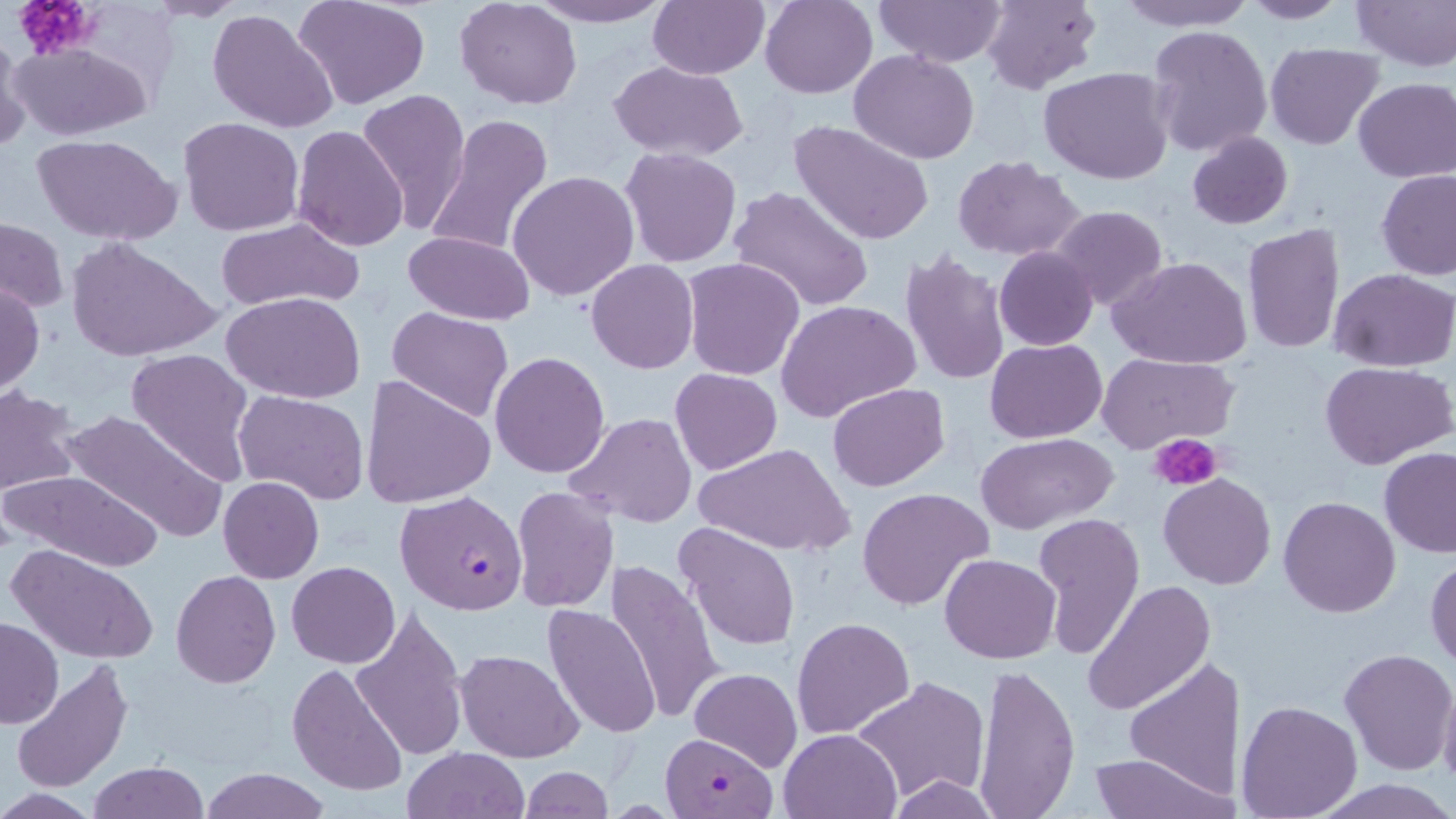 Approximate bounding boxes as (x1,y1)-(x2,y2) corner pairs in pixels. Plasmodium falciparum-infected red blood cell locations: (394,489)-(530,615), (662,732)-(775,816). Uninfected red blood cell locations: (141,0)-(247,21), (527,0)-(674,28), (648,0)-(768,79), (760,0)-(877,98), (872,0)-(1006,67), (979,0)-(1101,92), (1112,0)-(1257,30), (1351,0)-(1456,70), (293,1)-(433,111), (454,1)-(583,109), (1238,1)-(1353,23), (209,7)-(339,134), (1147,24)-(1271,157), (0,31)-(29,151), (8,41)-(154,142), (1264,42)-(1384,149), (850,50)-(980,164), (608,61)-(750,162), (1039,65)-(1173,185), (1353,78)-(1456,184), (355,88)-(471,232), (425,114)-(553,258), (177,117)-(305,237), (789,120)-(936,246), (290,126)-(410,251), (1186,131)-(1293,230), (32,132)-(184,246), (623,148)-(742,267), (954,157)-(1085,260), (508,169)-(641,302), (1377,169)-(1456,280), (729,187)-(876,314), (1051,205)-(1170,311), (214,218)-(366,312), (1,219)-(68,314), (1242,224)-(1347,357), (401,230)-(537,326), (65,237)-(221,364), (994,246)-(1098,351), (898,249)-(1012,390), (1110,256)-(1252,369), (681,257)-(806,381), (586,259)-(698,374), (1331,269)-(1456,371), (0,281)-(45,395), (223,292)-(367,404), (777,300)-(920,422), (386,307)-(513,423), (985,338)-(1107,442), (125,348)-(255,483), (490,351)-(611,477), (1098,353)-(1240,454), (1321,361)-(1455,469), (669,368)-(782,475), (360,374)-(496,509), (828,383)-(948,492), (1,385)-(81,499), (232,390)-(370,505), (57,407)-(226,543), (565,413)-(696,529), (975,433)-(1117,533), (697,441)-(851,558), (1378,447)-(1456,558), (3,467)-(163,572), (1159,473)-(1275,589), (218,477)-(323,583), (510,486)-(619,612), (857,488)-(993,612), (1278,497)-(1401,618), (1031,511)-(1145,660), (674,522)-(800,652), (5,543)-(158,665), (940,553)-(1060,665), (1426,556)-(1456,672), (604,558)-(725,724), (286,561)-(400,669), (171,571)-(281,689), (1083,581)-(1215,716), (543,604)-(663,740), (350,606)-(468,761), (791,616)-(914,740), (0,617)-(63,729), (455,646)-(584,762), (1338,646)-(1456,777), (11,658)-(133,794), (1124,659)-(1241,799), (288,662)-(410,798), (973,663)-(1081,819), (689,667)-(802,772), (1437,673)-(1456,793), (851,676)-(990,805), (1236,699)-(1364,817), (779,727)-(902,819), (402,747)-(528,818), (1086,752)-(1230,819), (87,762)-(210,818), (519,766)-(613,819), (198,769)-(330,819), (0,790)-(99,819). Platelet locations: (12,0)-(100,60), (1150,433)-(1224,492). Slide-level diagnosis: Plasmodium falciparum. Captured at 1000x magnification. Optical microscopy. Image is 1456×819 pixels. May-Grünwald-Giemsa-stained preparation. Thin blood smear. One field of a larger specimen.